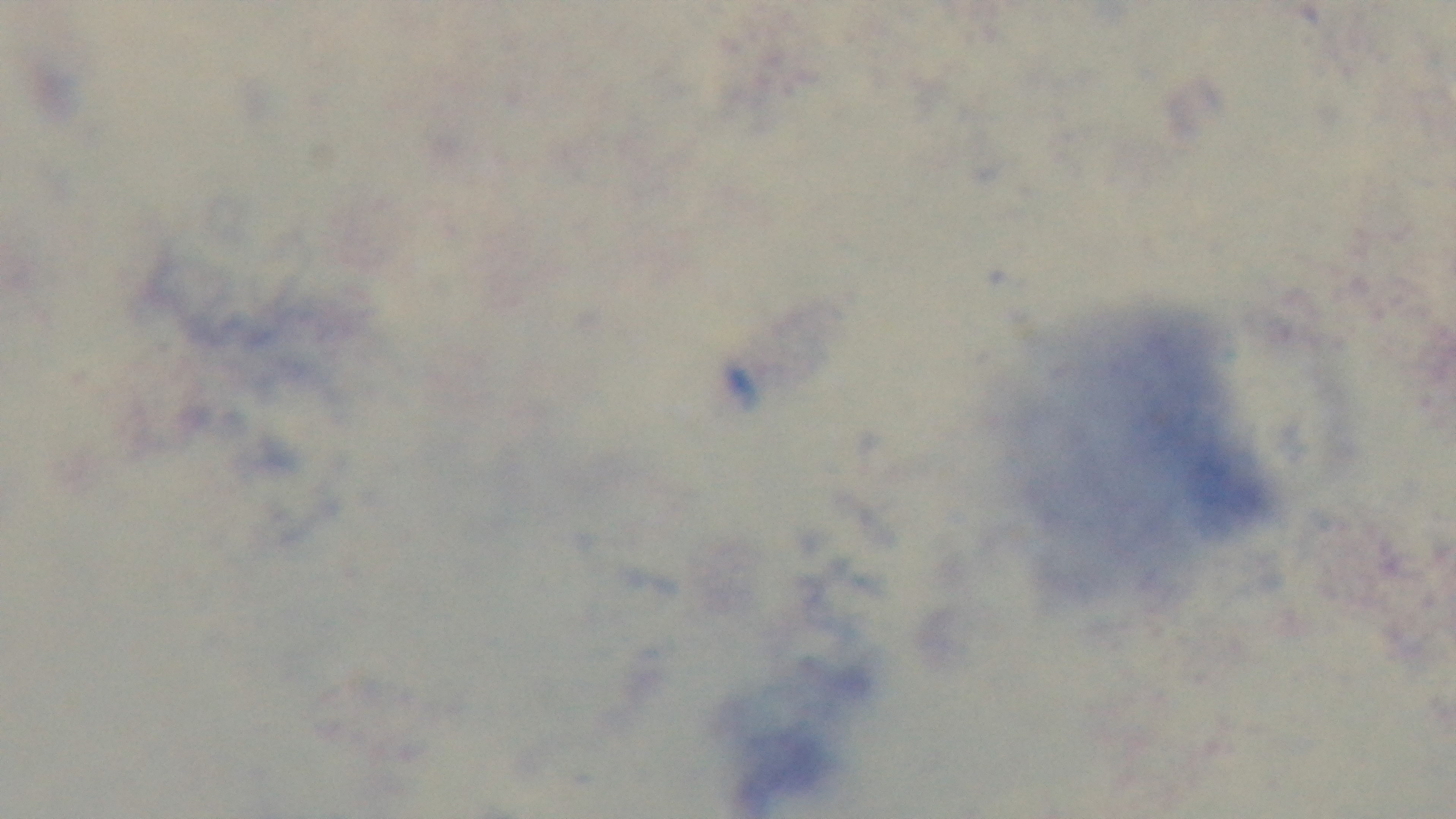
stain = Giemsa
field of view = one from the slide
malaria status = uninfected
objective = 100x oil immersion
modality = light microscopy
preparation = thick blood film
capture = mounted 4K digital camera